State which parasite is depicted.
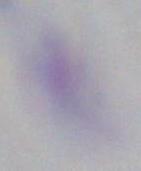

This is Toxoplasma gondii.

magnification: 1000x
modality: photomicrograph